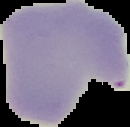
Malaria status: uninfected. From a thin blood film. Cell region segmented out of the field of view; the surrounding area is masked to black. Image is 130×127 pixels.